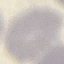
result = negative for malaria parasites
stain = Giemsa
image type = automatically extracted cell patch, resized to 64 × 64 pixels
preparation = thin blood smear
capture = smartphone camera at the microscope eyepiece